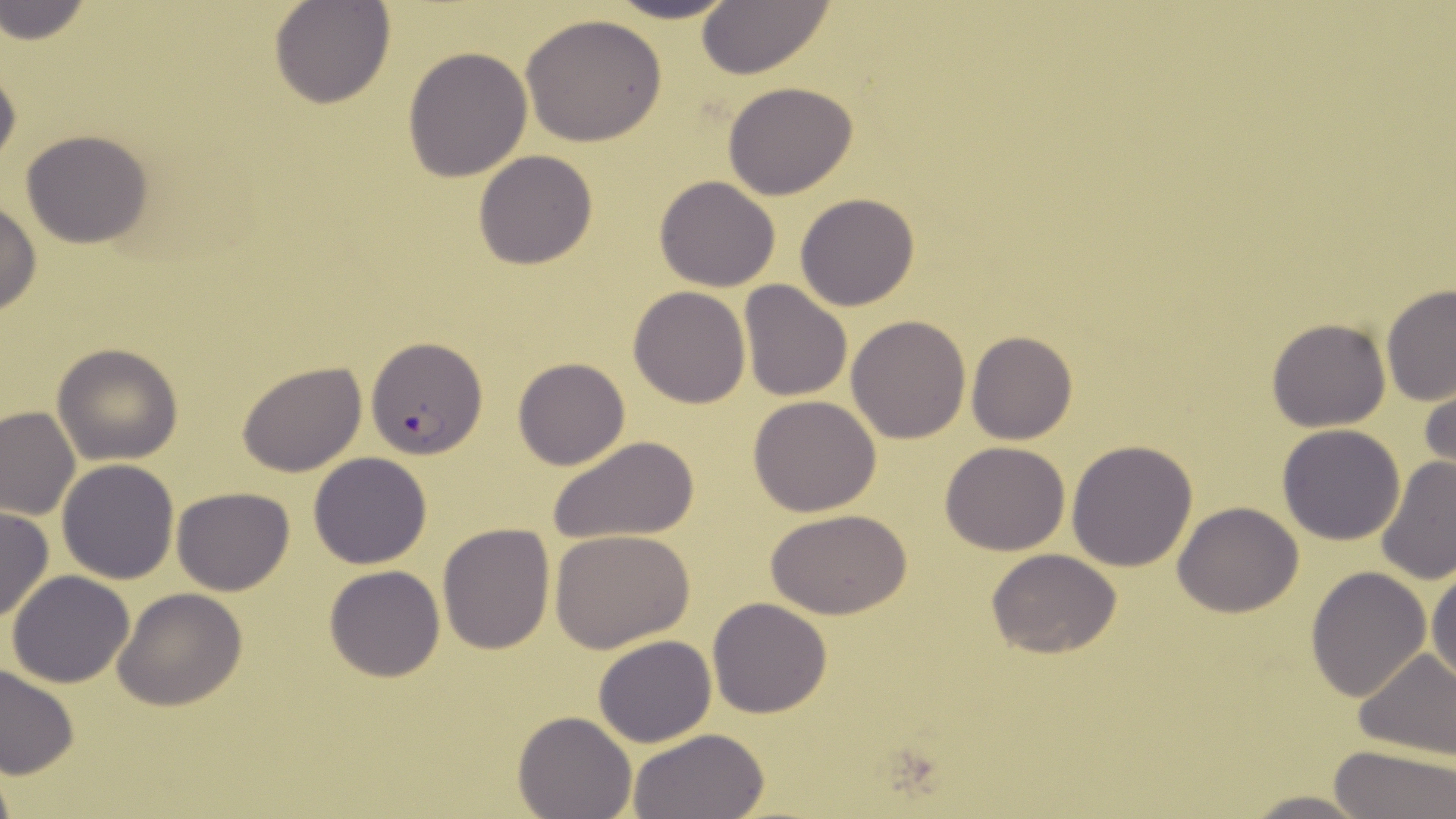
Summary:
  - Coordinate format: approximate bounding boxes as named x1/y1/x2/y2 corners in pixels
  - Plasmodium falciparum-infected red blood cell locations: (x1=366, y1=336, x2=488, y2=458)
  - Uninfected red blood cell locations: (x1=270, y1=0, x2=396, y2=110), (x1=600, y1=0, x2=744, y2=24), (x1=1, y1=1, x2=92, y2=45), (x1=694, y1=1, x2=838, y2=79), (x1=520, y1=14, x2=667, y2=145), (x1=402, y1=46, x2=533, y2=181), (x1=0, y1=52, x2=22, y2=174), (x1=722, y1=81, x2=860, y2=200), (x1=20, y1=130, x2=156, y2=248), (x1=473, y1=150, x2=598, y2=269), (x1=654, y1=175, x2=781, y2=292), (x1=795, y1=193, x2=922, y2=311), (x1=0, y1=199, x2=42, y2=318), (x1=738, y1=279, x2=854, y2=404), (x1=1381, y1=285, x2=1456, y2=408), (x1=627, y1=287, x2=751, y2=407), (x1=845, y1=315, x2=971, y2=443), (x1=1266, y1=317, x2=1390, y2=431), (x1=966, y1=330, x2=1078, y2=444), (x1=52, y1=344, x2=183, y2=464), (x1=513, y1=357, x2=631, y2=470), (x1=236, y1=361, x2=367, y2=478), (x1=1419, y1=368, x2=1456, y2=486), (x1=747, y1=394, x2=881, y2=515), (x1=0, y1=405, x2=80, y2=520), (x1=1277, y1=424, x2=1406, y2=546), (x1=552, y1=434, x2=699, y2=544), (x1=1066, y1=438, x2=1199, y2=573), (x1=940, y1=441, x2=1070, y2=556), (x1=308, y1=452, x2=433, y2=569), (x1=1376, y1=455, x2=1456, y2=587), (x1=57, y1=459, x2=180, y2=584), (x1=172, y1=487, x2=294, y2=596), (x1=1172, y1=500, x2=1305, y2=617), (x1=0, y1=506, x2=53, y2=624), (x1=767, y1=508, x2=914, y2=619), (x1=438, y1=522, x2=555, y2=654), (x1=549, y1=529, x2=696, y2=652), (x1=986, y1=548, x2=1123, y2=660), (x1=1428, y1=564, x2=1456, y2=687), (x1=323, y1=565, x2=447, y2=682), (x1=1306, y1=567, x2=1433, y2=703), (x1=6, y1=570, x2=135, y2=689), (x1=112, y1=587, x2=247, y2=711), (x1=708, y1=598, x2=833, y2=718), (x1=593, y1=635, x2=717, y2=748), (x1=1351, y1=649, x2=1456, y2=760), (x1=0, y1=663, x2=81, y2=781), (x1=513, y1=711, x2=636, y2=819), (x1=626, y1=727, x2=769, y2=818), (x1=1329, y1=745, x2=1456, y2=818), (x1=1238, y1=790, x2=1373, y2=819)
  - Slide-level diagnosis: Plasmodium falciparum
  - Image size: 1456×819 pixels
  - Stain: May-Grünwald-Giemsa
  - Preparation: thin blood smear
  - Modality: light microscopy
  - Field of view: one of a larger specimen
  - Magnification: 1000x